Give the extent of all uninfected red blood cells.
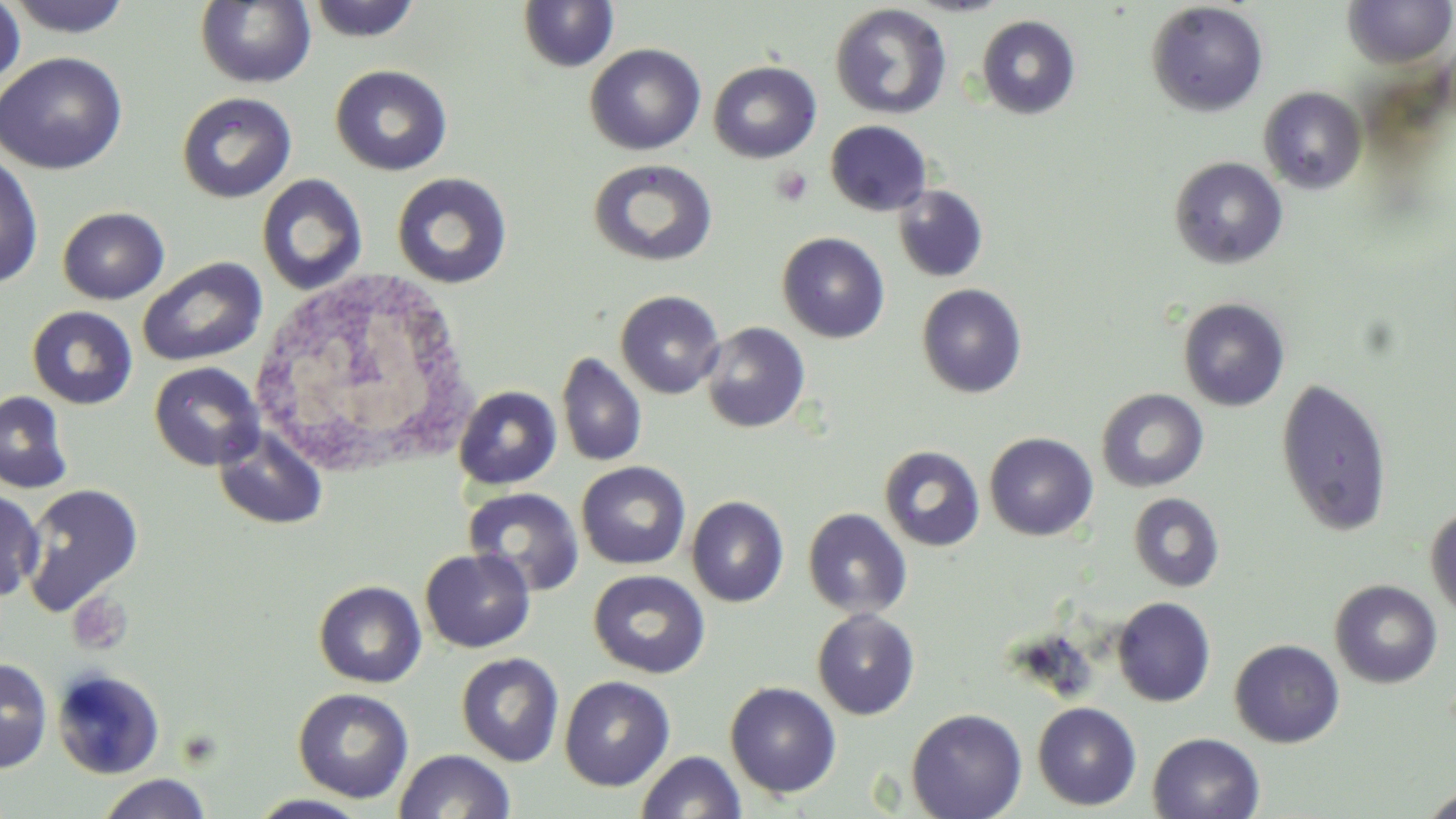

Approximate bounding boxes as [x1, y1, x2, y2] in pixels.
Uninfected red blood cells: [305, 0, 422, 42], [518, 0, 620, 73], [1342, 0, 1456, 68], [0, 1, 26, 93], [3, 1, 135, 38], [195, 1, 316, 89], [1145, 2, 1268, 117], [829, 3, 952, 120], [976, 15, 1081, 120], [584, 43, 706, 155], [0, 52, 127, 174], [707, 60, 821, 163], [330, 64, 452, 175], [1259, 87, 1367, 194], [175, 91, 297, 204], [825, 120, 932, 216], [0, 151, 44, 289], [1169, 156, 1288, 269], [588, 158, 717, 267], [391, 172, 513, 288], [257, 173, 368, 295], [892, 184, 989, 283], [57, 207, 170, 304], [777, 232, 890, 343], [137, 256, 267, 367], [916, 283, 1027, 398], [615, 290, 725, 399], [1177, 297, 1290, 412], [26, 306, 139, 410], [700, 322, 810, 433], [556, 352, 647, 468], [149, 362, 264, 471], [1276, 377, 1392, 536], [454, 385, 562, 490], [1096, 389, 1208, 492], [0, 390, 74, 495], [212, 425, 328, 531], [984, 432, 1099, 541], [879, 445, 985, 552], [576, 461, 691, 569], [20, 483, 143, 616], [463, 486, 584, 596], [0, 488, 44, 603], [1128, 493, 1225, 592], [686, 496, 789, 607], [1425, 504, 1456, 620], [803, 508, 912, 619], [420, 548, 535, 653], [589, 570, 710, 678], [1329, 579, 1443, 689], [313, 580, 426, 688], [1112, 597, 1216, 707], [812, 608, 920, 720], [1229, 639, 1345, 748], [456, 652, 564, 767], [0, 657, 53, 773], [456, 663, 672, 773], [51, 668, 165, 780], [559, 675, 675, 791], [725, 681, 841, 798], [293, 687, 414, 803], [1032, 702, 1142, 810], [906, 708, 1028, 819], [1147, 732, 1265, 819], [394, 749, 516, 818], [636, 750, 746, 819], [95, 773, 213, 819], [1419, 787, 1456, 818], [245, 792, 373, 818].

Summary:
  - Platelet locations: [771, 167, 813, 206], [66, 590, 133, 655]
  - White blood cell locations: [247, 270, 486, 472]
  - Slide-level diagnosis: negative for blood parasites
  - Field of view: one of a larger specimen
  - Preparation: thin blood smear
  - Magnification: 1000x
  - Image size: 1456×819 pixels
  - Stain: May-Grünwald-Giemsa
  - Modality: light microscopy